Name the blood parasite species.
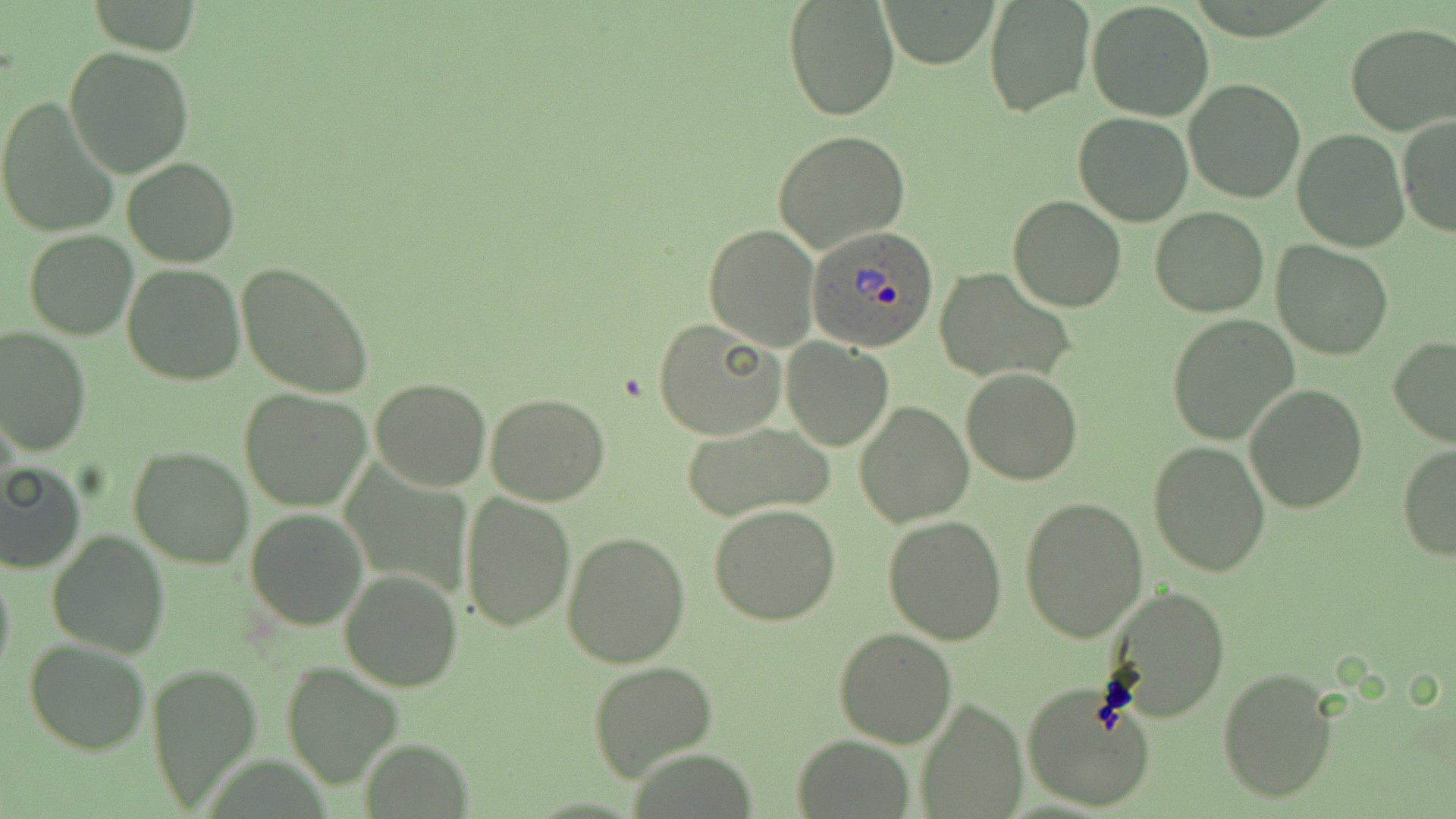

Plasmodium ovale.

magnification = 1000x
uninfected red blood cell locations = approximate bounding boxes as [x1, y1, x2, y2] in pixels: [783, 0, 900, 121], [881, 1, 997, 68], [1086, 1, 1215, 121], [983, 2, 1093, 118], [1345, 24, 1456, 135], [64, 46, 194, 178], [1183, 79, 1305, 204], [0, 97, 120, 239], [1073, 111, 1194, 226], [1397, 115, 1456, 239], [1292, 128, 1409, 251], [773, 129, 910, 255], [122, 157, 239, 268], [1008, 195, 1127, 312], [1151, 206, 1269, 316], [702, 223, 819, 351], [24, 231, 138, 339], [1271, 239, 1394, 360], [236, 261, 375, 398], [122, 263, 245, 385], [933, 266, 1074, 384], [1165, 316, 1298, 445], [653, 319, 785, 439], [0, 326, 92, 456], [1388, 336, 1456, 448], [781, 339, 894, 451], [961, 367, 1083, 485], [370, 377, 491, 491], [1244, 383, 1368, 515], [239, 389, 371, 512], [486, 391, 610, 506], [856, 401, 973, 527], [679, 419, 834, 523], [1148, 441, 1271, 576], [1396, 445, 1456, 561], [128, 446, 254, 567], [0, 460, 87, 574], [460, 493, 576, 631], [1020, 495, 1148, 643], [709, 505, 841, 625], [244, 508, 369, 630], [882, 515, 1008, 644], [46, 530, 170, 659], [562, 530, 690, 667], [0, 558, 15, 686], [339, 568, 465, 693], [1102, 585, 1234, 723], [833, 627, 959, 747], [23, 638, 151, 754], [146, 660, 262, 812], [587, 660, 719, 782], [281, 661, 401, 788], [1216, 667, 1340, 805], [1021, 682, 1157, 814], [917, 696, 1026, 819], [793, 735, 911, 817], [360, 737, 473, 818]
image size = 1456×819 pixels
modality = light microscopy
Plasmodium ovale-infected red blood cell locations = approximate bounding boxes as [x1, y1, x2, y2] in pixels: [806, 224, 938, 353]
stain = May-Grünwald-Giemsa
field of view = single
preparation = thin blood smear